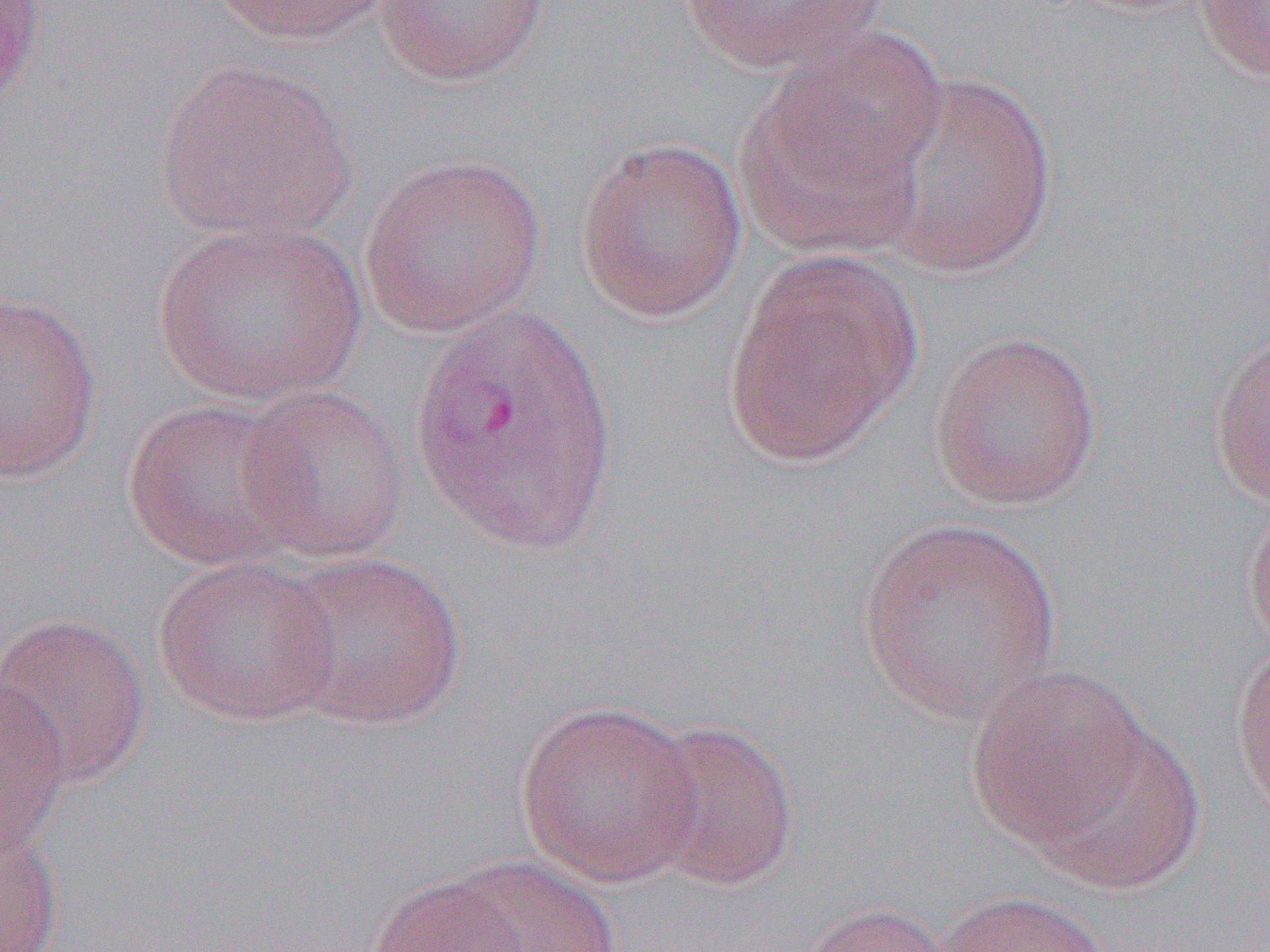

slide-level diagnosis = Plasmodium vivax
field of view = one of a larger specimen
uninfected red blood cell locations = approximate bounding boxes as [x1, y1, x2, y2] in pixels: [0, 0, 45, 114], [208, 0, 398, 46], [673, 0, 894, 74], [1195, 0, 1270, 83], [373, 1, 550, 86], [153, 58, 357, 245], [737, 58, 938, 258], [865, 71, 1059, 279], [574, 137, 749, 323], [358, 153, 547, 338], [154, 217, 368, 406], [721, 252, 922, 467], [0, 288, 102, 483], [1207, 327, 1270, 508], [929, 330, 1102, 510], [235, 385, 412, 564], [121, 397, 313, 571], [1242, 498, 1270, 657], [857, 516, 1064, 729], [272, 549, 467, 731], [153, 554, 344, 726], [0, 613, 151, 788], [1230, 642, 1270, 818], [965, 665, 1152, 849], [0, 672, 71, 863], [514, 699, 704, 887], [637, 718, 801, 892], [1028, 719, 1205, 892], [0, 826, 64, 951], [443, 855, 622, 952], [368, 873, 530, 952], [937, 890, 1118, 952], [791, 901, 959, 952]
magnification = 1000x
image size = 1270×952 pixels
modality = light microscopy
preparation = thin blood smear